Classify this cell by malaria status.
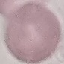

Uninfected.

Giemsa-stained preparation. Photographed with a smartphone camera at the microscope eyepiece. Thin blood smear. Cell patch, automatically extracted from a larger field of view and resized to 64 × 64 pixels.